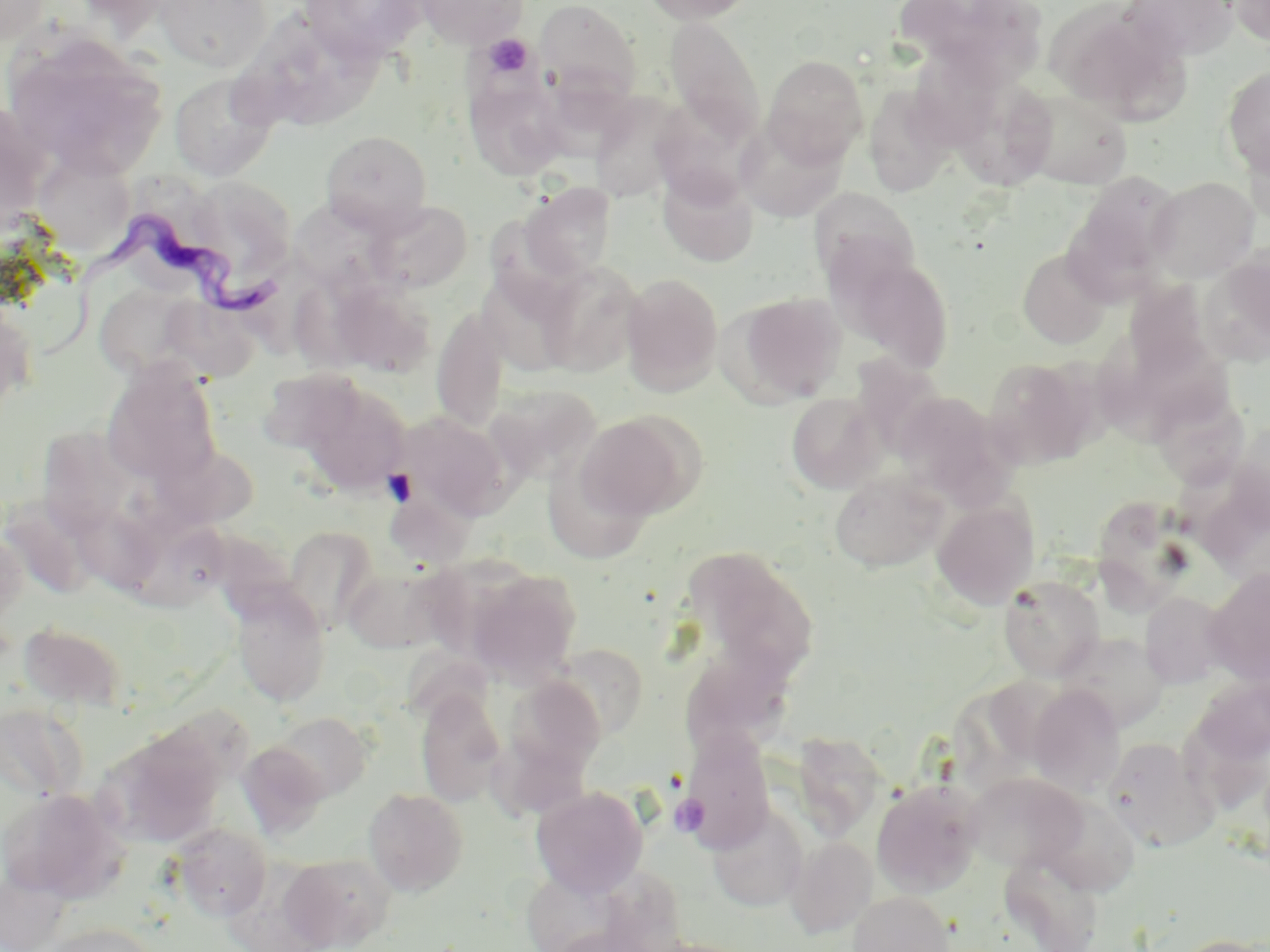
Summary:
  - Coordinate format: approximate bounding boxes as (x1, y1, x2, y2) in pixels
  - Uninfected red blood cell locations: (0, 0, 53, 47), (154, 0, 273, 72), (414, 0, 529, 48), (535, 0, 642, 105), (637, 0, 758, 25), (892, 0, 1044, 79), (1119, 0, 1238, 61), (1230, 0, 1270, 49), (300, 1, 430, 64), (1047, 3, 1183, 120), (665, 16, 766, 146), (277, 29, 398, 129), (4, 31, 169, 178), (911, 40, 1014, 146), (762, 54, 869, 166), (1221, 66, 1270, 178), (170, 71, 279, 182), (463, 71, 568, 181), (959, 84, 1059, 193), (863, 86, 956, 198), (1015, 88, 1135, 189), (590, 93, 690, 205), (735, 117, 847, 222), (320, 131, 432, 233), (31, 150, 135, 257), (657, 165, 758, 267), (1067, 171, 1185, 293), (1146, 177, 1259, 282), (518, 182, 617, 281), (809, 189, 920, 291), (365, 199, 473, 293), (295, 203, 394, 295), (1017, 248, 1113, 349), (1205, 248, 1270, 363), (839, 252, 955, 374), (538, 261, 643, 376), (288, 272, 395, 373), (621, 273, 724, 395), (619, 279, 842, 396), (1120, 281, 1218, 389), (338, 282, 443, 382), (96, 285, 194, 378), (729, 292, 847, 406), (161, 297, 260, 383), (0, 304, 36, 419), (432, 305, 509, 434), (982, 357, 1099, 469), (101, 359, 222, 487), (1102, 361, 1202, 447), (255, 367, 366, 456), (298, 381, 410, 495), (485, 384, 601, 485), (893, 391, 1013, 505), (786, 392, 884, 494), (1162, 396, 1253, 494), (396, 411, 511, 522), (576, 412, 701, 521), (43, 428, 137, 540), (151, 442, 259, 531), (541, 459, 661, 562), (830, 470, 949, 572), (397, 476, 483, 564), (931, 497, 1040, 610), (1096, 500, 1191, 617), (128, 516, 234, 613), (282, 525, 379, 633), (0, 529, 28, 630), (685, 547, 821, 681), (342, 561, 454, 655), (465, 566, 581, 686), (1204, 568, 1270, 685), (998, 575, 1104, 681), (229, 585, 332, 707), (1140, 592, 1231, 689), (17, 621, 129, 713), (1057, 632, 1169, 732), (536, 648, 643, 746), (683, 651, 796, 766), (506, 673, 609, 777), (1027, 685, 1126, 796), (415, 688, 507, 807), (0, 703, 88, 801), (271, 712, 373, 802), (101, 728, 224, 848), (679, 730, 776, 851), (792, 733, 888, 842), (1103, 736, 1220, 853), (237, 740, 330, 839), (964, 772, 1087, 872), (871, 778, 984, 897), (531, 786, 648, 898), (0, 787, 128, 903), (363, 788, 468, 896), (1037, 794, 1140, 896), (706, 803, 809, 912), (172, 822, 271, 921), (786, 836, 878, 938), (1000, 850, 1105, 951), (280, 852, 396, 950), (519, 866, 630, 952), (0, 868, 72, 952), (848, 891, 955, 952), (40, 923, 161, 952), (1171, 934, 1270, 952)
  - Platelet locations: (483, 34, 533, 79), (671, 794, 709, 836)
  - Trypanosoma brucei locations: (47, 210, 289, 369)
  - Slide-level diagnosis: Trypanosoma brucei
  - Stain: May-Grünwald-Giemsa
  - Field of view: one of a larger specimen
  - Preparation: thin blood film
  - Image size: 1270×952 pixels
  - Modality: optical microscopy
  - Magnification: 1000x